Report the malaria status of this cell.
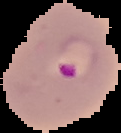
Parasitized.

Image is 121×133 pixels. Segmented cell region on a black background. From a thin blood smear.